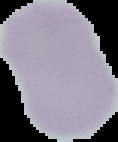

Summary:
  - Preparation: thin blood smear
  - Image size: 118×142 pixels
  - Image type: segmented cell region on a black background
  - Result: negative for malaria parasites